Give the extent of all Plasmodium malariae-infected red blood cells.
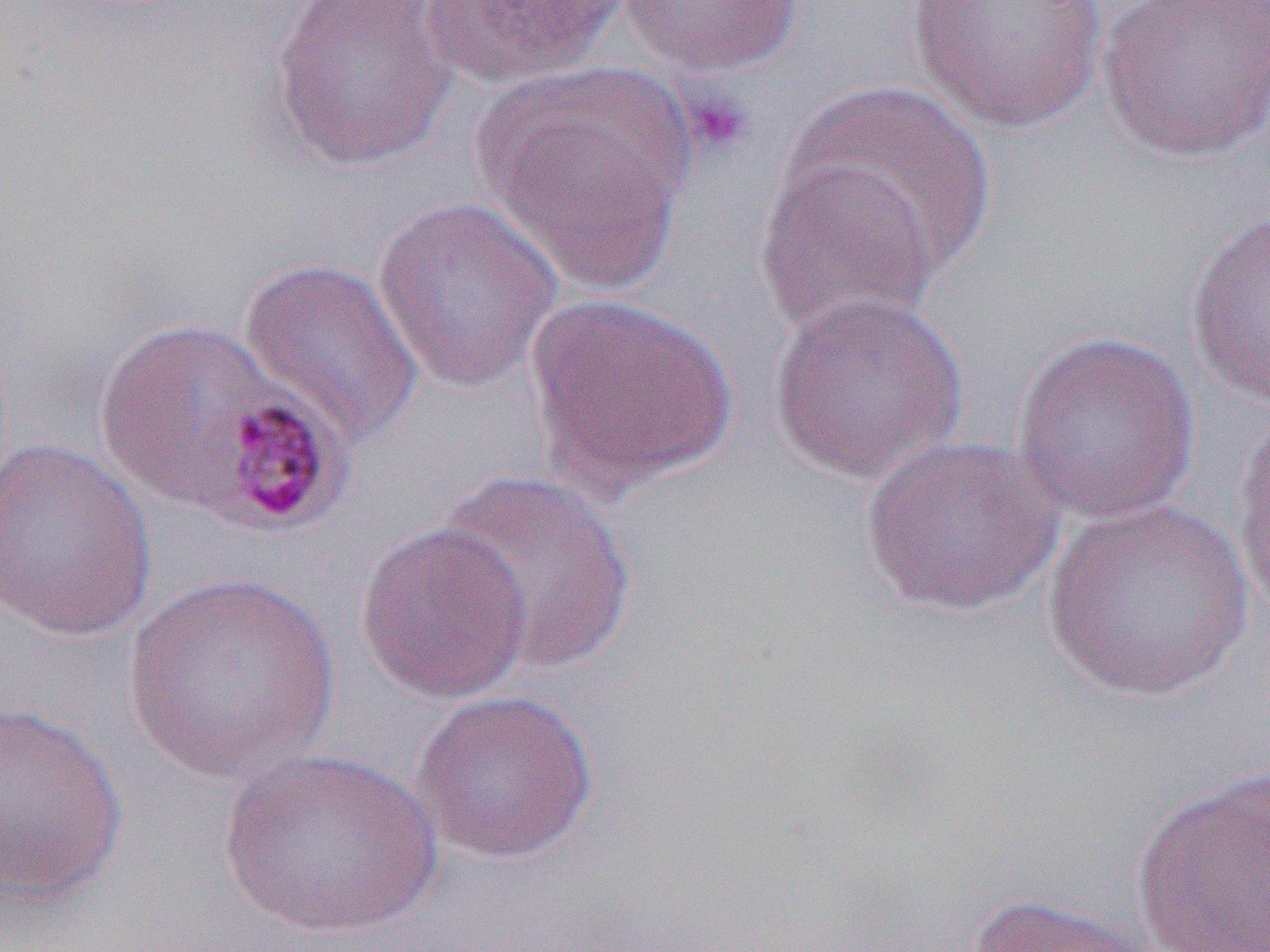

Approximate bounding boxes as (x1,y1)-(x2,y2) corner pairs in pixels.
Plasmodium malariae-infected red blood cells: (204,392)-(357,535).

slide_level_diagnosis: Plasmodium malariae
image_size: 1270×952 pixels
platelet_locations: 'approximate bounding boxes as (x1,y1)-(x2,y2) corner pairs in pixels: (682,91)-(753,157)'
magnification: 1000x
modality: light microscopy
uninfected_red_blood_cell_locations: 'approximate bounding boxes as (x1,y1)-(x2,y2) corner pairs in pixels: (266,0)-(459,172), (616,0)-(803,74), (908,0)-(1107,133), (1098,0)-(1269,163), (417,1)-(628,87), (480,68)-(693,296), (782,82)-(995,279), (755,152)-(945,342), (371,197)-(564,391), (1185,211)-(1270,407), (237,256)-(424,447), (768,290)-(969,485), (521,293)-(737,498), (94,315)-(309,521), (1012,331)-(1201,523), (1231,404)-(1270,618), (859,434)-(1065,618), (1,437)-(158,643), (435,470)-(638,677), (1039,499)-(1258,702), (355,520)-(533,705), (124,572)-(340,785), (410,690)-(599,865), (0,700)-(128,907), (219,748)-(443,938), (1131,767)-(1270,952), (966,892)-(1174,952)'
field_of_view: single
preparation: thin blood smear